Name the parasite shown.
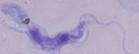

A trypanosome.

modality = photomicrograph
magnification = 1000x